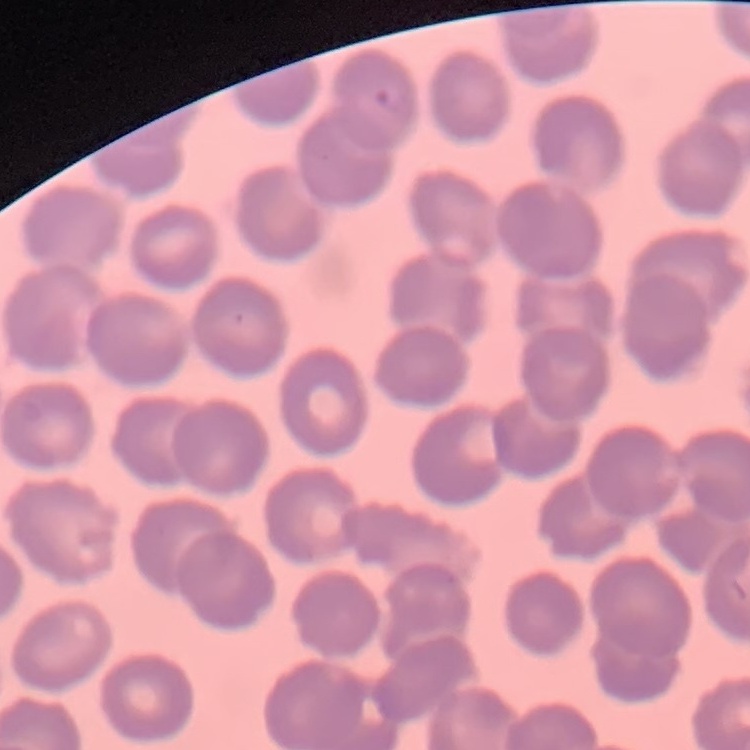 The erythrocytes exhibit no rouleaux formation. Square crop of a larger photomicrograph. Field's or Giemsa stain. Thin blood film.